Assess the morphology of the erythrocytes.
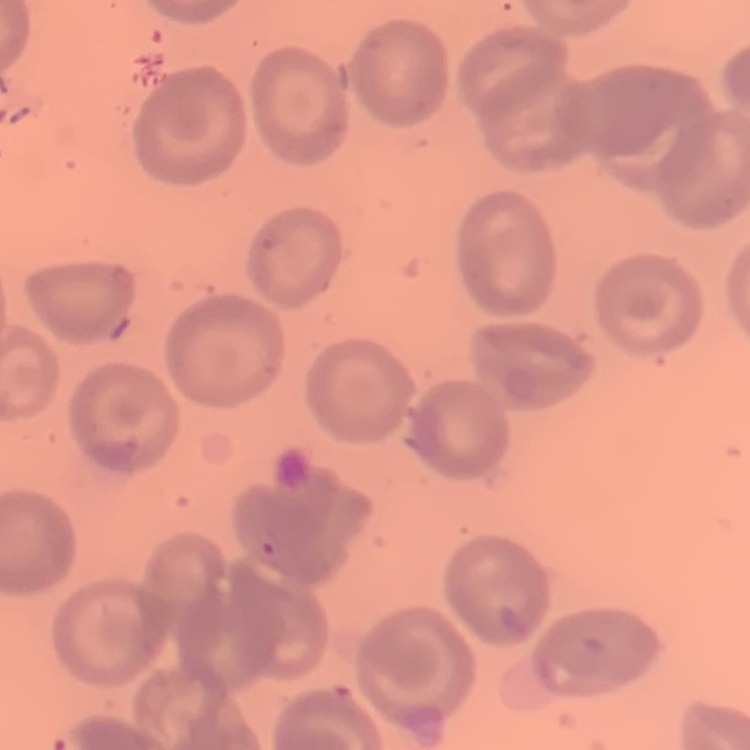
They show no rouleaux formation.

image type = square crop of a larger photomicrograph
preparation = thin blood smear
stain = Field's or Giemsa